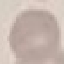

Result: negative for malaria parasites. Giemsa-stained preparation. Thin blood film. Cell patch, automatically extracted from a larger field of view and resized to 64 × 64 pixels. Photographed with a smartphone camera at the microscope eyepiece.